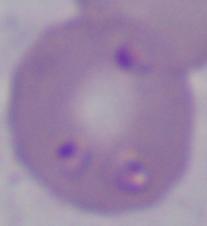
A Babesia parasite is seen. Micrograph. 1000x magnification.